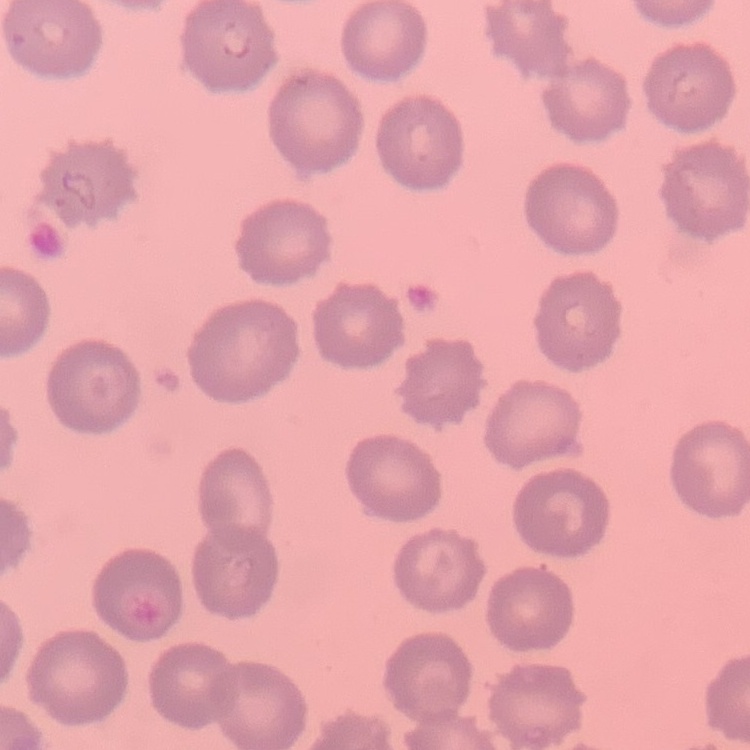
The red blood cells show no rouleaux formation. One tile cut from a larger photomicrograph. Field's or Giemsa stain. Thin peripheral smear.